Locate every Plasmodium falciparum-infected red blood cell.
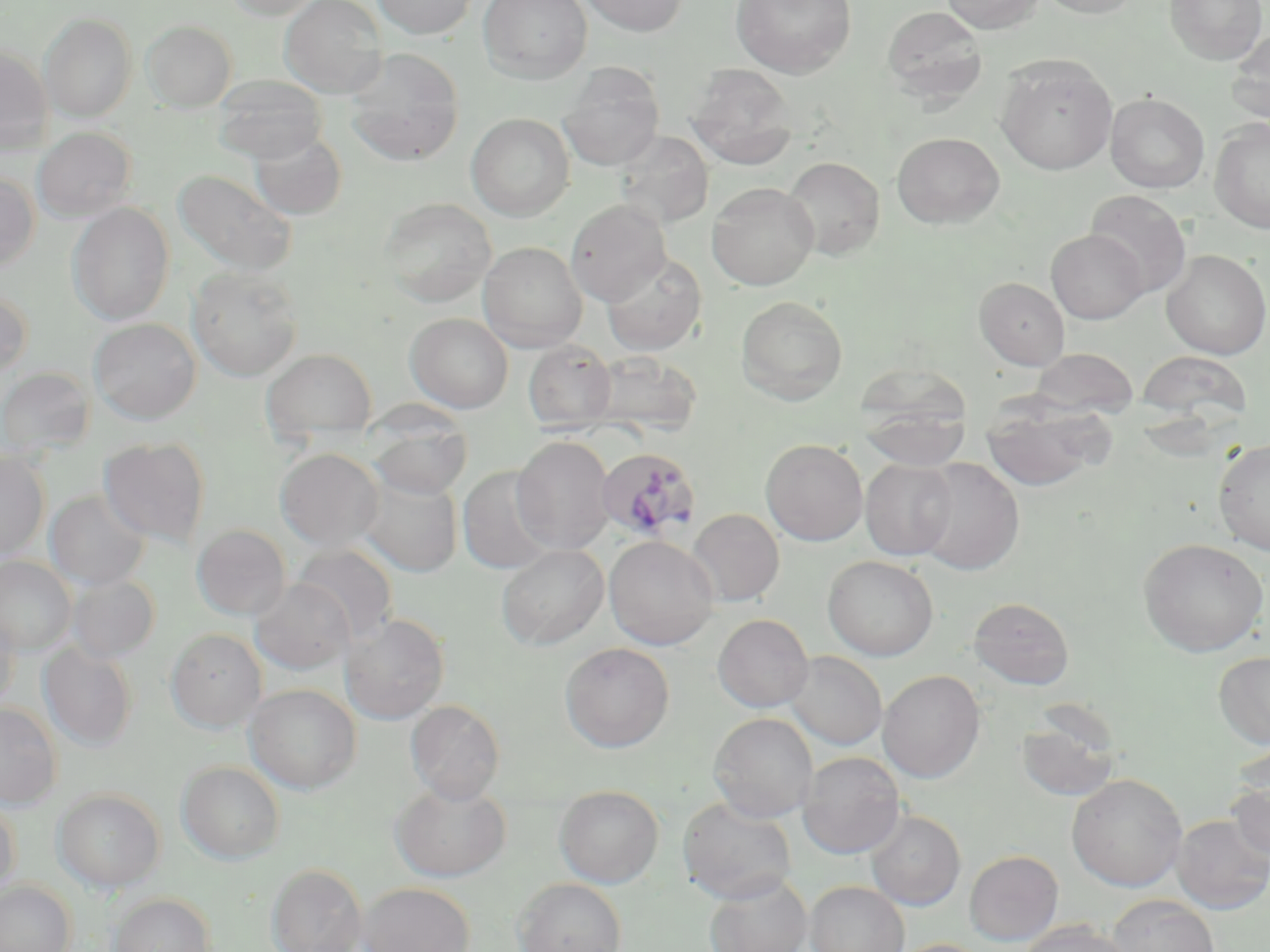
Approximate bounding boxes as (x1,y1)-(x2,y2) corner pairs in pixels.
Plasmodium falciparum-infected red blood cells: (597,447)-(702,541).

Uninfected red blood cell locations: (224,0)-(328,20), (280,0)-(388,99), (371,0)-(477,39), (477,0)-(592,83), (577,0)-(689,37), (730,0)-(857,79), (942,0)-(1045,34), (1037,0)-(1142,19), (1165,0)-(1267,65), (881,5)-(988,103), (39,12)-(138,121), (142,20)-(237,112), (1227,29)-(1270,128), (0,45)-(52,153), (344,49)-(464,167), (996,54)-(1117,175), (559,64)-(665,171), (685,64)-(801,170), (212,75)-(328,163), (1106,93)-(1209,193), (466,113)-(574,221), (1210,118)-(1270,234), (32,127)-(136,223), (249,131)-(347,220), (615,131)-(713,228), (892,132)-(1005,228), (782,156)-(885,260), (173,170)-(297,277), (0,172)-(40,271), (707,182)-(818,290), (1084,190)-(1192,298), (379,198)-(496,307), (566,199)-(671,305), (68,203)-(174,325), (1046,229)-(1148,323), (479,241)-(587,352), (1161,250)-(1269,359), (601,253)-(707,356), (187,266)-(304,381), (974,277)-(1069,370), (0,287)-(33,380), (735,296)-(848,404), (406,313)-(513,413), (89,318)-(201,424), (523,340)-(617,432), (1029,348)-(1140,417), (261,349)-(376,440), (586,350)-(703,439), (1136,350)-(1253,424), (0,367)-(95,458), (858,370)-(971,471), (982,397)-(1110,492), (368,417)-(472,500), (512,435)-(615,555), (98,437)-(211,547), (1213,438)-(1270,556), (760,439)-(868,545), (275,448)-(384,552), (0,451)-(50,560), (913,458)-(1025,575), (860,459)-(958,560), (458,465)-(557,574), (358,473)-(463,577), (45,489)-(151,590), (688,509)-(785,606), (191,524)-(291,620), (604,535)-(719,650), (1138,537)-(1269,656), (496,544)-(609,650), (292,545)-(399,644), (822,555)-(939,660), (0,556)-(76,654), (66,573)-(160,663), (249,578)-(354,674), (968,596)-(1075,690), (0,610)-(20,711), (712,613)-(813,713), (341,614)-(450,724), (165,628)-(266,732), (38,642)-(138,750), (559,642)-(675,752), (785,651)-(887,750), (1214,651)-(1270,748), (878,670)-(985,783), (244,684)-(361,794), (405,700)-(505,804), (0,703)-(62,808), (1015,711)-(1121,803), (708,712)-(818,822), (798,751)-(905,858), (177,761)-(285,864), (1067,773)-(1187,892), (1227,774)-(1270,864), (390,781)-(511,882), (554,784)-(664,888), (53,788)-(165,892), (678,797)-(797,903), (0,798)-(21,899), (866,810)-(966,911), (1170,814)-(1270,913), (964,850)-(1063,946), (266,863)-(367,952), (703,873)-(812,952), (513,878)-(627,952), (0,880)-(76,952), (805,881)-(909,952), (359,882)-(475,952), (108,892)-(216,952), (1107,894)-(1219,952), (1019,920)-(1132,952), (891,938)-(989,952). Slide-level diagnosis: Plasmodium falciparum. Light microscopy. Captured at 1000x magnification. Image is 1270×952 pixels. Thin blood smear. May-Grünwald-Giemsa-stained preparation. One field of a larger specimen.